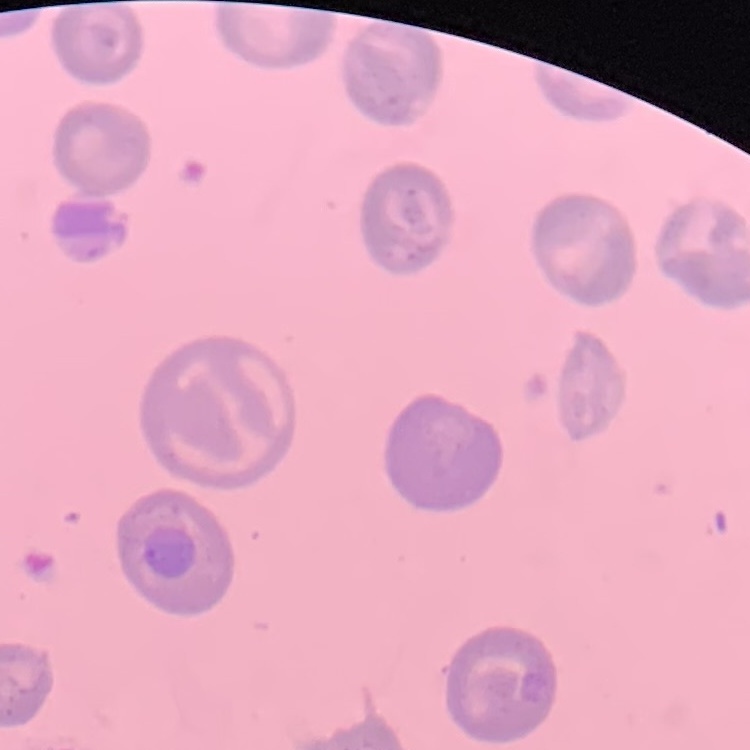

erythrocyte morphology = no rouleaux formation
image type = one tile cut from a larger photomicrograph
preparation = thin peripheral smear
stain = Field's or Giemsa